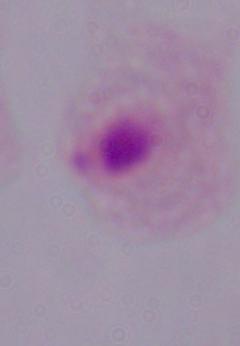
identification = trichomonad
magnification = 1000x
modality = photomicrograph